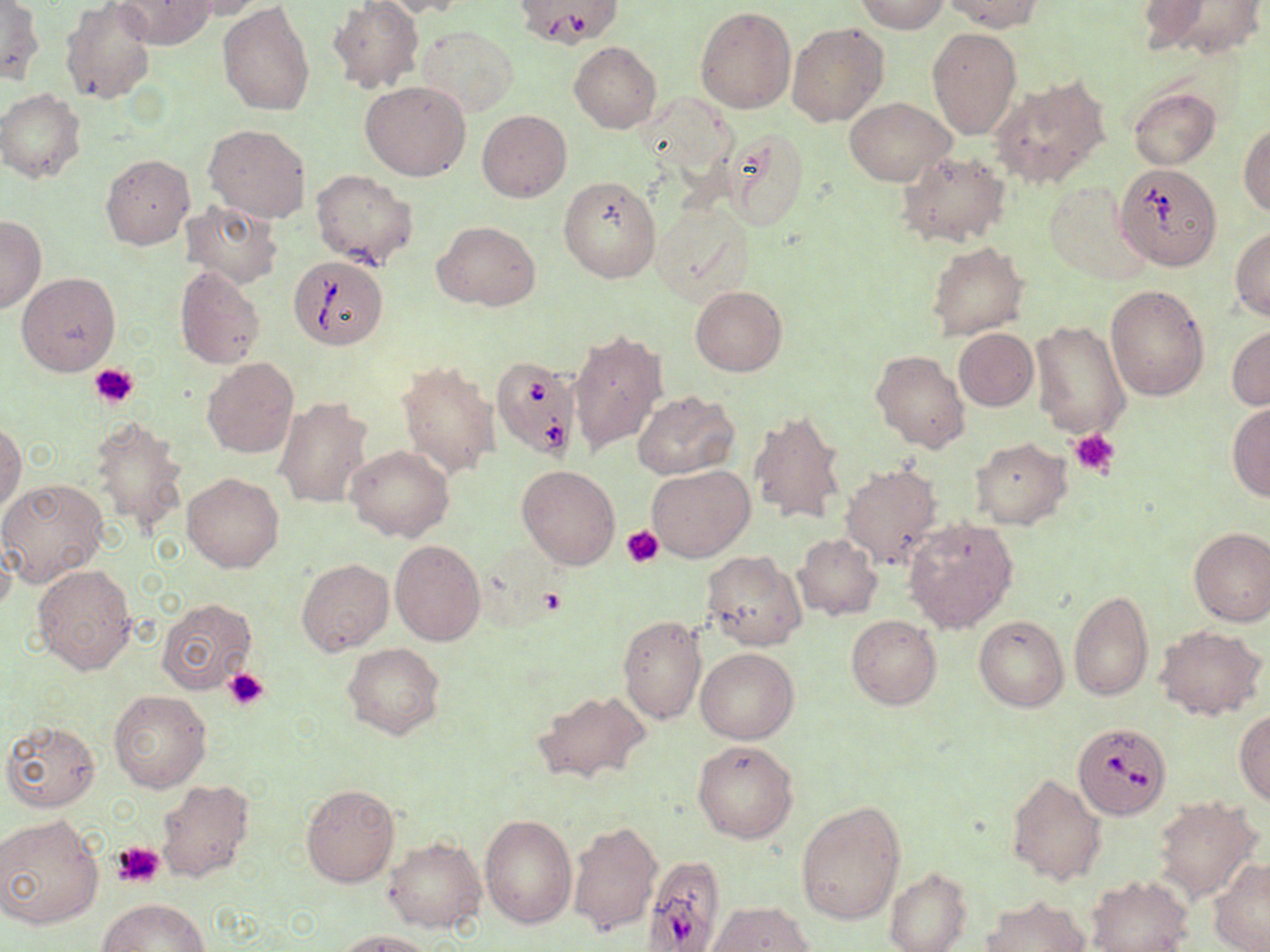

Approximate bounding boxes as (x1, y1, x2, y2) in pixels. Uninfected red blood cell locations: (60, 0, 156, 104), (179, 0, 266, 19), (373, 0, 475, 18), (855, 0, 950, 34), (941, 0, 1042, 32), (1, 1, 44, 84), (112, 1, 218, 50), (218, 1, 314, 115), (328, 1, 423, 94), (1134, 1, 1212, 51), (1163, 2, 1264, 58), (694, 7, 796, 114), (788, 22, 888, 126), (417, 25, 519, 117), (926, 27, 1022, 140), (569, 42, 661, 133), (991, 77, 1109, 190), (361, 79, 472, 181), (1, 88, 86, 183), (1129, 88, 1220, 169), (844, 97, 953, 185), (478, 110, 572, 201), (205, 123, 311, 223), (1239, 123, 1269, 216), (720, 129, 811, 229), (896, 150, 1011, 249), (100, 153, 194, 249), (311, 168, 418, 268), (559, 176, 660, 284), (1043, 179, 1151, 285), (182, 198, 283, 288), (652, 199, 756, 306), (0, 216, 45, 313), (433, 222, 539, 309), (1230, 227, 1270, 320), (927, 242, 1028, 339), (175, 265, 265, 370), (16, 271, 121, 376), (1105, 284, 1211, 401), (689, 285, 786, 376), (1031, 319, 1129, 439), (1227, 325, 1270, 411), (954, 328, 1037, 410), (569, 329, 669, 454), (871, 349, 970, 453), (201, 357, 298, 459), (397, 361, 499, 480), (633, 390, 740, 481), (275, 397, 372, 509), (1226, 402, 1270, 501), (749, 407, 851, 528), (90, 415, 187, 540), (0, 422, 24, 513), (970, 437, 1071, 529), (346, 445, 454, 543), (841, 463, 943, 569), (649, 464, 754, 561), (517, 466, 619, 569), (182, 472, 283, 572), (0, 477, 108, 587), (902, 516, 1019, 633), (1188, 527, 1270, 626), (793, 533, 882, 619), (390, 539, 485, 646), (701, 550, 805, 649), (296, 559, 393, 656), (32, 564, 136, 676), (1068, 590, 1153, 701), (156, 598, 259, 694), (846, 614, 942, 709), (618, 615, 706, 726), (974, 615, 1068, 711), (1156, 625, 1267, 721), (343, 643, 444, 740), (696, 647, 798, 744), (533, 688, 653, 786), (108, 690, 211, 792), (1235, 709, 1270, 803), (1, 719, 101, 813), (692, 740, 798, 843), (1007, 773, 1107, 885), (155, 778, 255, 884), (302, 784, 399, 887), (1154, 798, 1257, 900), (796, 801, 906, 927), (480, 813, 576, 927), (0, 814, 104, 931), (567, 819, 661, 938), (385, 836, 486, 933), (1210, 858, 1270, 952), (884, 867, 972, 952), (1087, 875, 1192, 952), (981, 896, 1090, 952), (100, 897, 210, 951), (709, 902, 814, 951), (337, 929, 437, 952). Babesia divergens-infected red blood cell locations: (513, 0, 620, 47), (1114, 164, 1221, 269), (289, 257, 387, 349), (491, 355, 582, 459), (1073, 722, 1174, 821), (645, 854, 731, 952). Platelet locations: (89, 363, 138, 409), (1070, 428, 1121, 478), (622, 525, 664, 567), (537, 586, 565, 616), (224, 668, 270, 712), (112, 841, 165, 888). Slide-level diagnosis: Babesia divergens. May-Grünwald-Giemsa-stained preparation. Light microscopy. Image is 1270×952 pixels. Thin blood smear. Single field of view. Captured at 1000x magnification.